Assess this cell for malaria.
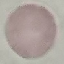

It is uninfected.

image type = automatically extracted cell patch, resized to 64 × 64 pixels
stain = Giemsa
capture = smartphone through the microscope eyepiece
preparation = thin blood smear